Outline each blood parasite and name the species.
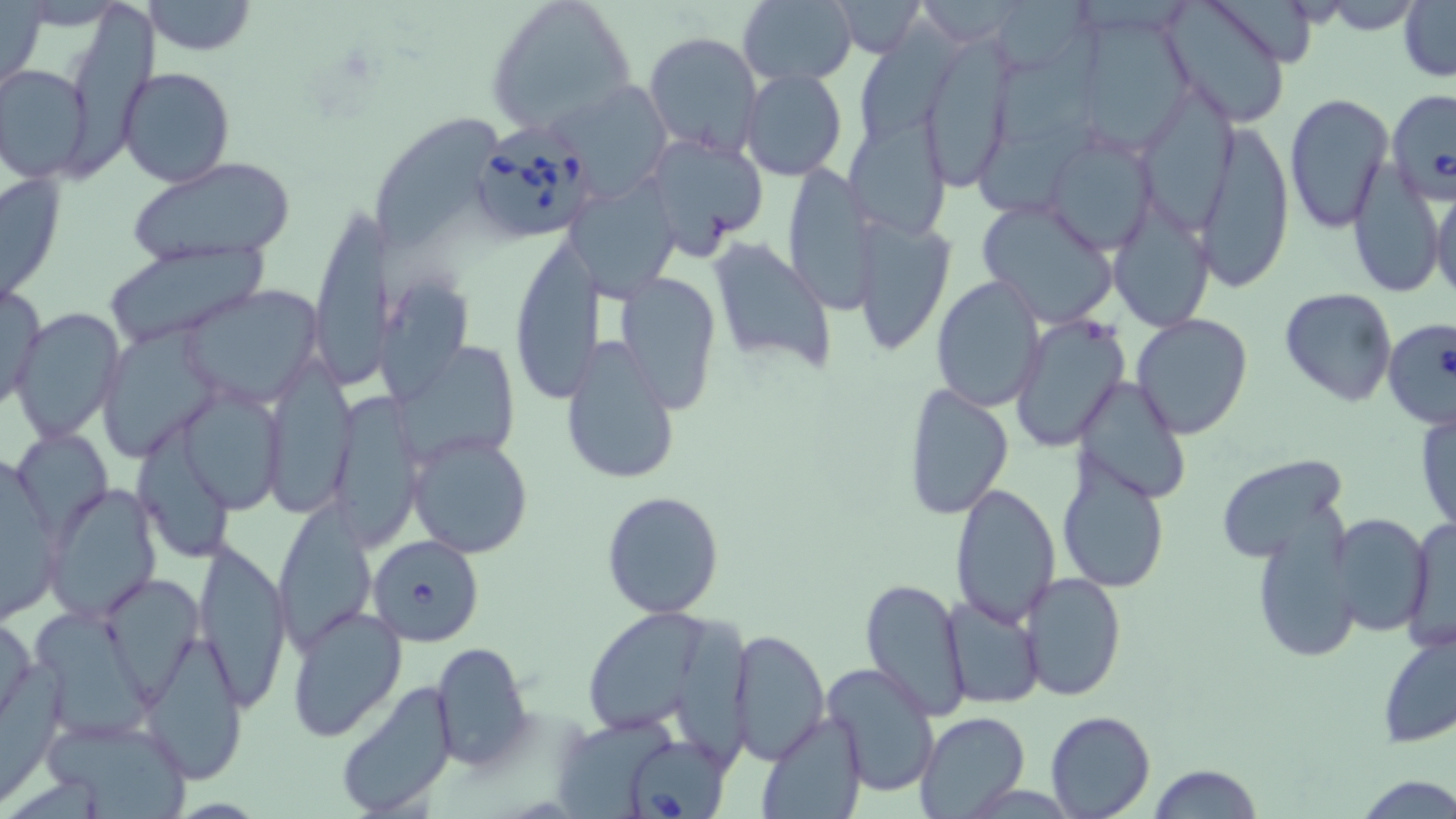
Approximate bounding boxes as (x1,y1)-(x2,y2) corner pairs in pixels.
Babesia divergens-infected red blood cells: (470,119)-(596,243), (1382,319)-(1456,429), (368,534)-(485,646), (623,734)-(734,817).
No Plasmodium falciparum, Plasmodium ovale, Plasmodium malariae, Plasmodium vivax, or Trypanosoma brucei observed.

slide-level diagnosis = Babesia divergens
image size = 1456×819 pixels
uninfected red blood cell locations = approximate bounding boxes as (x1,y1)-(x2,y2) corner pairs in pixels: (139,0)-(259,55), (486,0)-(635,132), (736,0)-(857,88), (832,1)-(923,57), (1159,1)-(1295,128), (1399,1)-(1455,83), (0,2)-(47,98), (71,2)-(157,183), (860,12)-(971,139), (1072,13)-(1197,153), (995,23)-(1109,150), (644,31)-(763,155), (925,44)-(1015,185), (1,63)-(93,183), (119,67)-(235,187), (740,67)-(848,180), (548,80)-(670,199), (1146,90)-(1250,229), (1385,90)-(1456,203), (1283,92)-(1394,232), (376,115)-(507,257), (852,121)-(957,240), (1192,121)-(1296,294), (978,125)-(1104,214), (643,132)-(767,255), (1042,133)-(1158,255), (127,157)-(298,265), (1349,161)-(1446,301), (780,162)-(878,312), (1,169)-(67,306), (568,171)-(682,297), (1431,186)-(1455,302), (976,199)-(1120,330), (1109,203)-(1216,333), (310,204)-(386,390), (850,217)-(955,356), (508,235)-(601,403), (706,235)-(837,370), (99,243)-(273,347), (613,272)-(722,414), (931,275)-(1045,411), (383,279)-(477,407), (1,281)-(46,411), (180,284)-(325,408), (1279,288)-(1397,406), (12,306)-(124,444), (1132,313)-(1254,441), (1009,315)-(1129,452), (103,320)-(215,463), (561,336)-(680,488), (391,343)-(522,457), (273,353)-(359,522), (1074,375)-(1190,505), (901,384)-(1014,520), (178,389)-(287,514), (326,390)-(424,550), (1414,404)-(1455,532), (23,425)-(118,537), (141,426)-(234,555), (406,430)-(533,559), (2,447)-(62,626), (1214,453)-(1352,565), (1055,456)-(1171,595), (949,481)-(1061,628), (43,483)-(162,624), (602,490)-(727,619), (271,501)-(376,650), (1327,511)-(1436,637), (1401,515)-(1455,654), (1250,522)-(1360,662), (192,538)-(292,709), (100,571)-(203,696), (1020,571)-(1126,702), (860,577)-(971,720), (941,595)-(1045,709), (286,603)-(409,741), (583,606)-(700,740), (32,607)-(153,740), (1,613)-(36,727), (682,620)-(753,769), (1376,625)-(1456,748), (730,629)-(829,763), (141,637)-(249,784), (431,642)-(531,770), (824,661)-(939,796), (333,680)-(459,818), (1045,710)-(1155,818), (756,711)-(867,819), (40,712)-(194,818), (915,712)-(1030,819), (551,716)-(680,819), (1147,765)-(1264,819)
stain = May-Grünwald-Giemsa
field of view = one of a larger specimen
modality = light microscopy
magnification = 1000x
preparation = thin blood smear